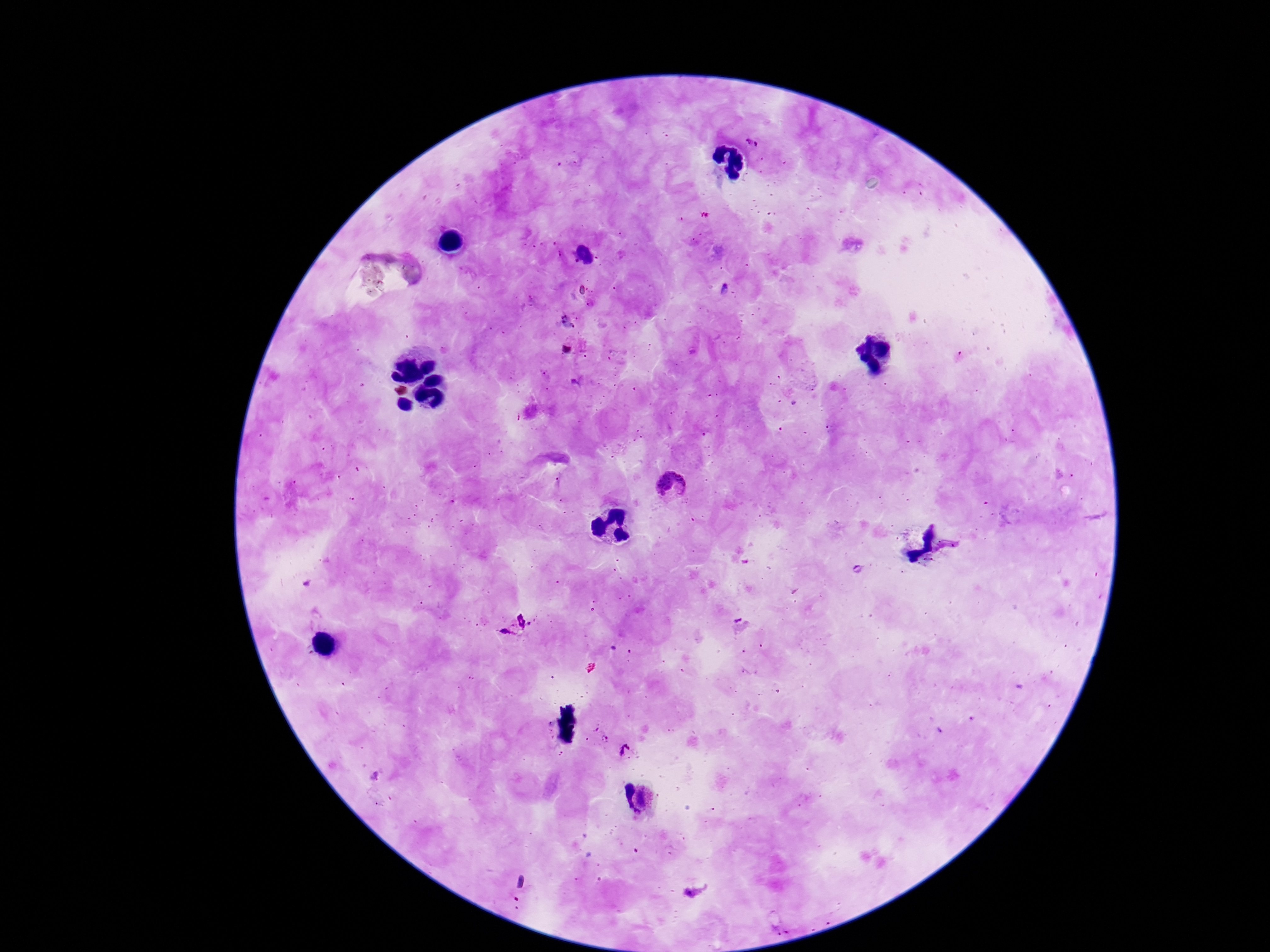
Approximate centers as [x, y] in pixels.
Summary:
  - Plasmodium parasite locations: [675, 486], [514, 624], [620, 749]
  - Patient malaria status: positive
  - Image size: 1270×952 pixels
  - Stain: Giemsa
  - Magnification: 100x
  - Field of view: single
  - Capture: smartphone camera through the microscope eyepiece
  - Preparation: thick peripheral-blood smear